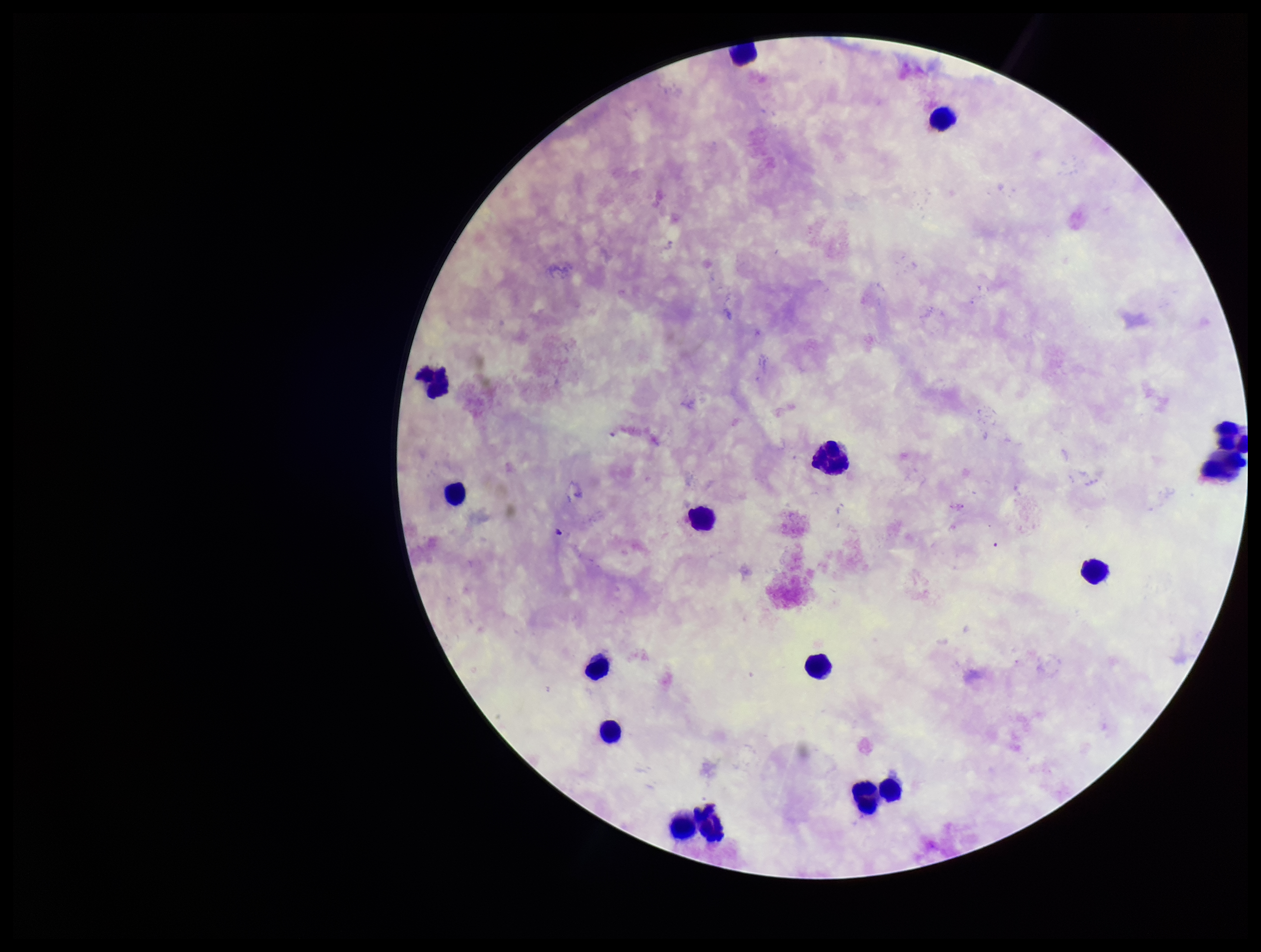
Patient malaria status: negative. Parasite count: 0. One field from this slide. Leukocyte count: 16. Smartphone photograph taken through the eyepiece of a microscope. Image is 1261×952 pixels. Stained with Giemsa. Plasmodium parasites: none seen. Preparation: thick blood smear.